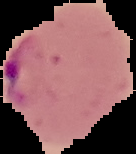
Result: Plasmodium parasites detected. From a thin blood smear. Image is 136×154 pixels. Cell region segmented out of the field of view; the surrounding area is masked to black.